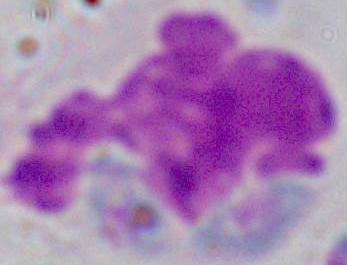
magnification = 1000x
modality = photomicrograph
identification = leukocyte